Name the parasite shown.
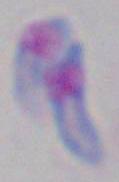
This is Toxoplasma gondii.

Photomicrograph. 1000x magnification.